Classify this cell by malaria status.
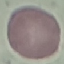

It is uninfected.

Cell patch, automatically extracted from a larger field of view and resized to 64 × 64 pixels. Giemsa stain. Thin blood film. Photographed with a smartphone camera at the microscope eyepiece.